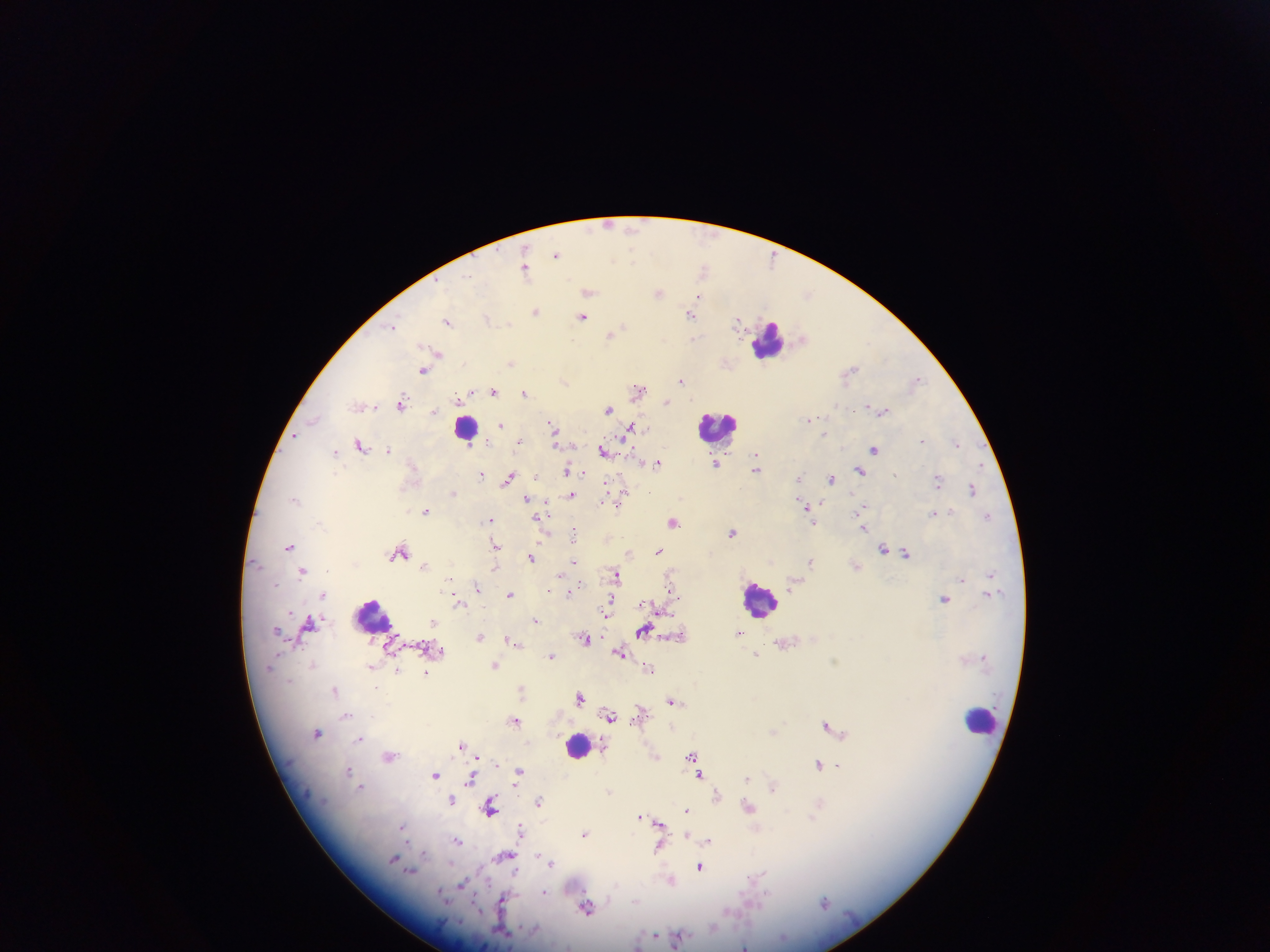

Plasmodium parasite locations = approximate centers as (x, y) in pixels: (608, 223), (557, 255), (525, 266), (704, 270), (588, 290), (659, 293), (700, 297), (693, 308), (535, 312), (691, 314), (584, 316), (487, 318), (448, 320), (738, 322), (392, 327), (612, 334), (804, 338), (438, 353), (512, 361), (725, 363), (424, 370), (850, 372), (917, 379), (682, 380), (565, 381), (639, 390), (494, 391), (525, 392), (459, 400), (667, 402), (401, 404), (365, 405), (608, 408), (882, 410), (434, 411), (810, 417), (502, 424), (553, 426), (631, 427), (824, 434), (295, 435), (519, 440), (923, 440), (957, 443), (361, 445), (558, 445), (875, 448), (388, 449), (603, 451), (336, 452), (756, 456), (716, 461), (657, 463), (758, 468), (860, 470), (568, 471), (583, 474), (482, 475), (536, 475), (510, 476), (798, 478), (831, 479), (939, 480), (608, 484), (973, 488), (624, 491), (454, 493), (572, 495), (528, 498), (604, 502), (613, 503), (821, 503), (807, 507), (862, 508), (426, 511), (934, 512), (988, 514), (490, 518), (537, 519), (673, 521), (814, 521), (864, 527), (732, 532), (574, 533), (495, 544), (290, 545), (884, 548), (402, 551), (660, 551), (629, 552), (905, 553), (532, 557), (574, 560), (811, 561), (424, 566), (856, 566), (494, 569), (302, 570), (560, 573), (990, 573), (616, 574), (962, 579), (672, 581), (794, 584), (477, 587), (569, 592), (323, 593), (988, 593), (510, 594), (945, 599), (460, 600), (612, 602), (610, 610), (606, 613), (535, 620), (434, 621), (311, 622), (645, 629), (740, 632), (680, 635), (480, 636), (585, 639), (512, 640), (518, 643), (785, 643), (621, 652), (757, 654), (552, 655), (495, 663), (371, 666), (649, 667), (399, 670), (426, 672), (522, 688), (336, 691), (580, 697), (673, 699), (641, 713), (346, 715), (610, 715), (515, 720), (828, 724), (774, 731), (318, 733), (360, 738), (462, 745), (389, 756), (654, 756), (693, 756), (478, 757), (696, 761), (496, 764), (819, 764), (837, 765), (349, 770), (436, 773), (518, 773), (700, 775), (748, 778), (471, 779), (362, 787), (773, 787), (608, 791), (716, 794), (452, 799), (539, 801), (490, 805), (820, 805), (750, 806), (687, 810), (641, 815), (659, 823), (402, 827), (522, 831), (659, 831), (585, 833), (687, 836), (710, 839), (458, 841), (660, 845), (506, 855), (551, 862), (700, 866), (757, 878), (671, 879), (462, 883), (545, 893), (503, 900), (825, 902), (587, 908), (657, 934), (678, 938), (638, 945), (744, 946)
country = Ghana
preparation = thick blood film
capture = mobile-phone photograph through a microscope
field of view = single
image size = 1270×952 pixels
leukocyte locations = approximate centers as (x, y) in pixels: (768, 340), (718, 425), (466, 427), (759, 598), (373, 616), (981, 719), (578, 745)